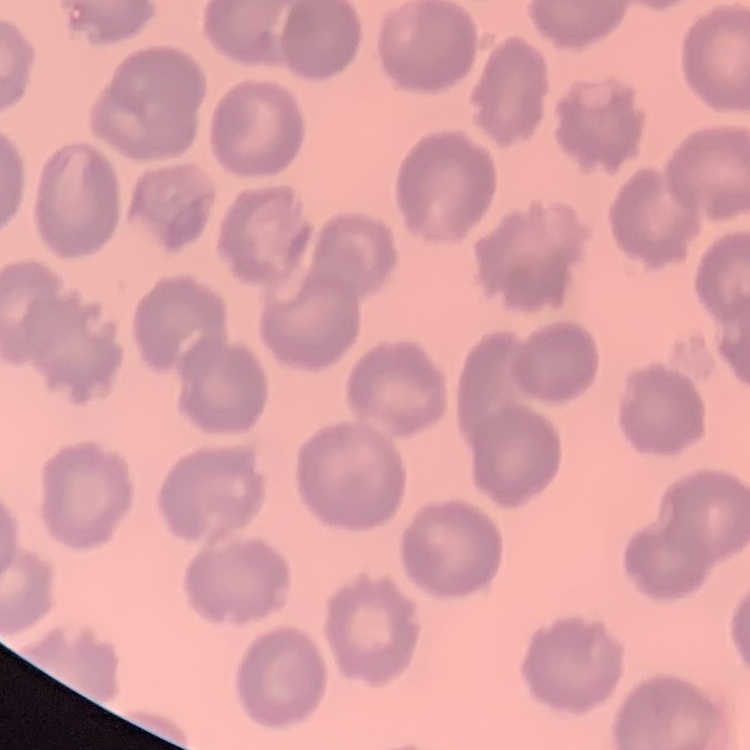

Summary:
  - Erythrocyte morphology: no rouleaux formation
  - Preparation: thin blood film
  - Image type: square crop of a larger photomicrograph
  - Stain: Field's or Giemsa